Assess the morphology of the erythrocytes.
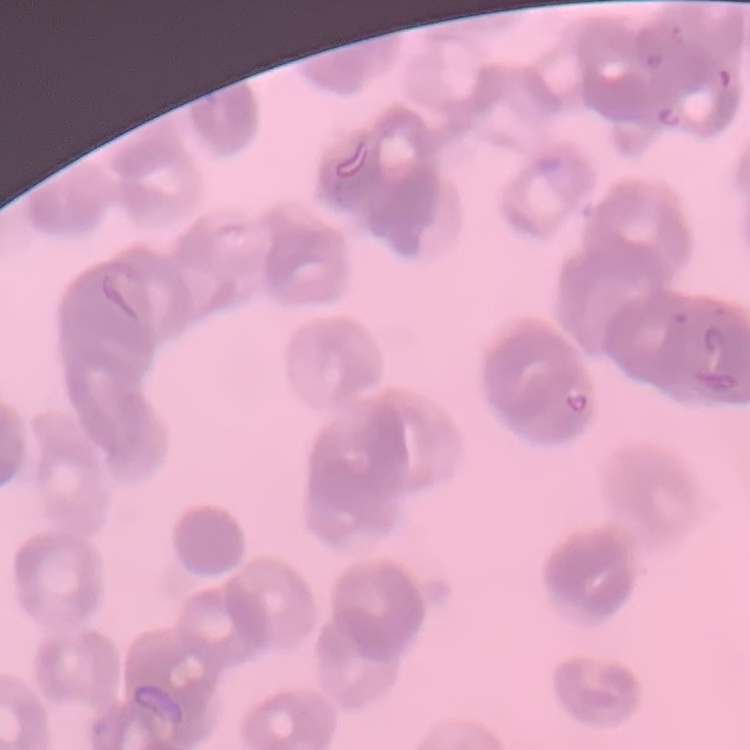
They show rouleaux formation.

One tile cut from a larger photomicrograph. Field's or Giemsa stain. Thin peripheral smear.